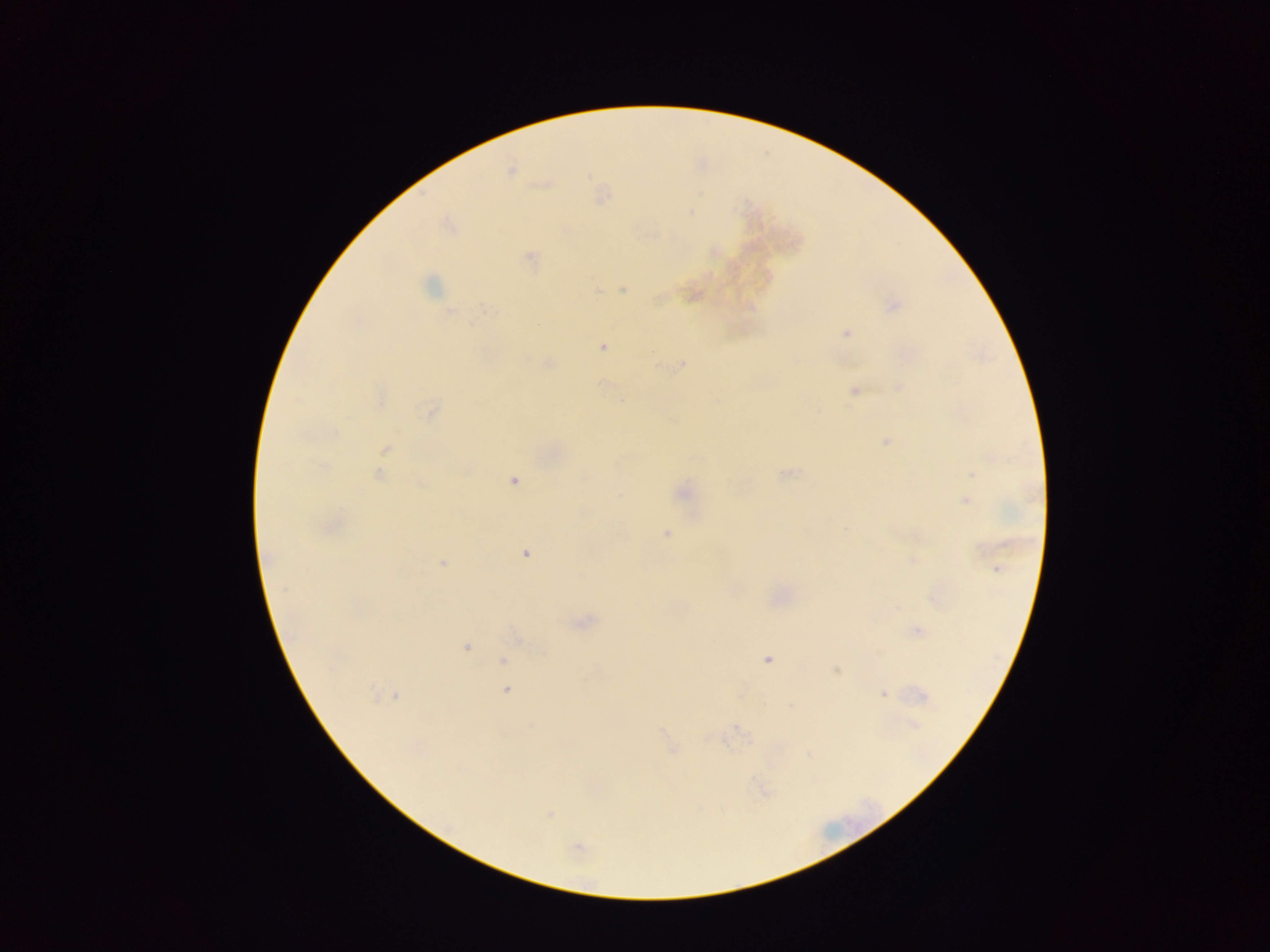 Approximate centers as [x, y] in pixels. Plasmodium parasite locations: [510, 170], [543, 184], [600, 195], [691, 211], [449, 224], [714, 252], [530, 258], [432, 285], [622, 289], [596, 290], [693, 294], [891, 306], [450, 311], [847, 333], [602, 346], [549, 362], [682, 362], [899, 388], [853, 390], [380, 399], [430, 411], [886, 439], [386, 449], [786, 472], [379, 473], [971, 473], [513, 479], [421, 484], [681, 492], [964, 500], [329, 525], [667, 533], [526, 553], [443, 563], [996, 568], [935, 595], [583, 622], [916, 630], [517, 638], [465, 645], [767, 659], [503, 660], [502, 668], [836, 670], [506, 690], [742, 692], [883, 694], [921, 695], [387, 696], [913, 724], [670, 749], [548, 815], [578, 849]. One field of view. Image is 1270×952 pixels. Photographed through a microscope with a mobile-phone camera. Thick blood film. Collected in Ghana.